Assess this cell for malaria.
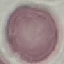
It is uninfected.

image_type: automatically extracted cell patch, resized to 64 × 64 pixels
preparation: thin smear
capture: smartphone camera at the microscope eyepiece
stain: Giemsa